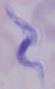
Micrograph. Captured at 1000x magnification. A trypanosome is shown.